Identify the parasite.
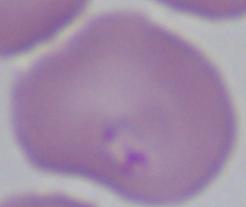
This is Babesia.

Summary:
  - Magnification: 1000x
  - Modality: micrograph